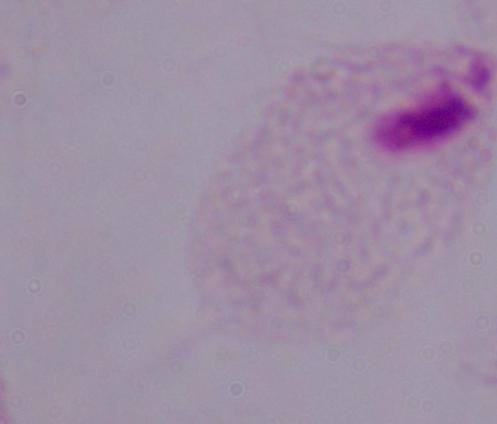
A trichomonad is shown. 1000x magnification. Micrograph.